Assess this cell for malaria.
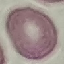
Uninfected.

Summary:
  - Stain: Giemsa
  - Preparation: thin blood smear
  - Image type: automatically extracted cell patch, resized to 64 × 64 pixels
  - Capture: smartphone camera at the microscope eyepiece